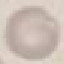
Summary:
  - Result: no malaria parasites seen
  - Image type: cell patch, automatically extracted from a larger field of view and resized to 64 × 64 pixels
  - Preparation: thin smear
  - Stain: Giemsa
  - Capture: smartphone camera at the microscope eyepiece